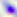

{
  "magnification": "400x",
  "identification": "Toxoplasma gondii",
  "modality": "photomicrograph"
}